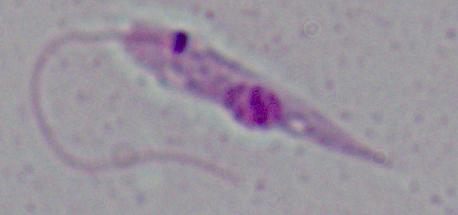 A Leishmania parasite is seen. Micrograph. 1000x magnification.